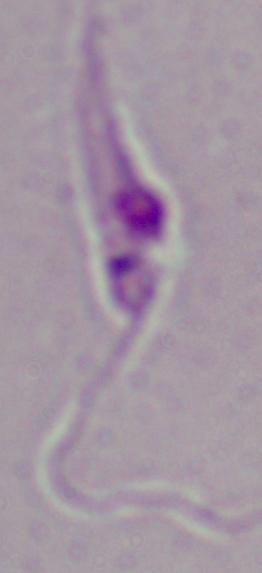

Captured at 1000x magnification. A Leishmania parasite is shown. Micrograph.